Assess this cell for malaria.
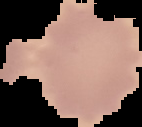

It is uninfected.

The area outside the segmented cell region is set to black. Image is 142×127 pixels. From a thin blood film.